Locate the cells, classifying each as a parasitized red blood cell, an uninfected red blood cell, or a white blood cell.
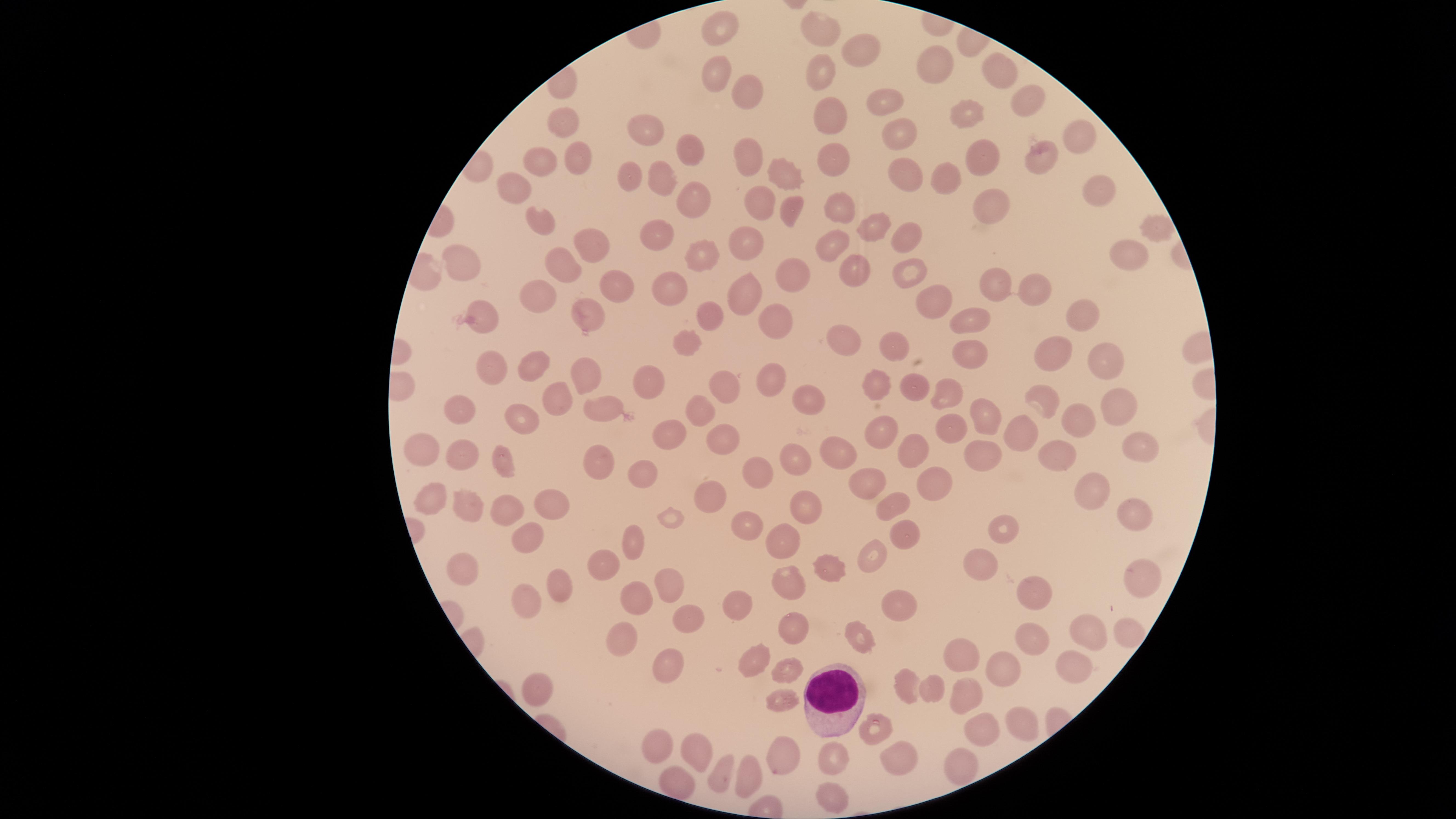

Approximate marker points, in pixels from the top-left corner.
Parasitized red blood cells: (x=876, y=722).
Uninfected red blood cells: (x=724, y=20), (x=823, y=29), (x=858, y=47), (x=933, y=61), (x=714, y=71), (x=818, y=71), (x=1004, y=71), (x=744, y=88), (x=1025, y=92), (x=885, y=104), (x=827, y=110), (x=557, y=115), (x=962, y=116), (x=643, y=127), (x=1081, y=134), (x=898, y=136), (x=682, y=149), (x=748, y=150), (x=987, y=151), (x=1037, y=156), (x=836, y=159), (x=537, y=163), (x=576, y=163), (x=784, y=169), (x=630, y=178), (x=941, y=178), (x=908, y=179), (x=660, y=180), (x=514, y=187), (x=1096, y=192), (x=685, y=194), (x=989, y=200), (x=758, y=205), (x=842, y=209), (x=790, y=213), (x=532, y=215), (x=872, y=228), (x=1157, y=234), (x=656, y=238), (x=905, y=238), (x=587, y=239), (x=835, y=246), (x=743, y=247), (x=707, y=253), (x=1127, y=256), (x=462, y=258), (x=563, y=261), (x=849, y=268), (x=909, y=272), (x=796, y=274), (x=998, y=281), (x=611, y=287), (x=1036, y=290), (x=674, y=291), (x=931, y=300), (x=748, y=302), (x=543, y=304), (x=708, y=314), (x=1084, y=314), (x=586, y=316), (x=488, y=317), (x=776, y=320), (x=966, y=325), (x=849, y=342), (x=693, y=344), (x=893, y=344), (x=971, y=357), (x=1059, y=359), (x=1110, y=366), (x=528, y=367), (x=493, y=368), (x=585, y=375), (x=650, y=378), (x=773, y=379), (x=726, y=382), (x=872, y=383), (x=910, y=391), (x=950, y=391), (x=560, y=398), (x=1045, y=399), (x=799, y=401), (x=1109, y=406), (x=463, y=407), (x=607, y=408), (x=701, y=409), (x=526, y=413), (x=1075, y=417), (x=990, y=418), (x=881, y=431), (x=948, y=431), (x=672, y=435), (x=1135, y=439), (x=1027, y=440), (x=722, y=441), (x=418, y=446), (x=912, y=447), (x=983, y=448), (x=455, y=451), (x=832, y=452), (x=1051, y=456), (x=794, y=458), (x=597, y=462), (x=505, y=465), (x=637, y=471), (x=756, y=477), (x=860, y=478), (x=937, y=485), (x=1089, y=493), (x=712, y=494), (x=426, y=498), (x=550, y=499), (x=1136, y=502), (x=887, y=505), (x=799, y=506), (x=469, y=507), (x=503, y=507), (x=749, y=523), (x=998, y=530), (x=902, y=534), (x=522, y=537), (x=785, y=538), (x=632, y=547), (x=874, y=555), (x=977, y=562), (x=607, y=564), (x=462, y=568), (x=1136, y=568), (x=833, y=569), (x=1036, y=582), (x=673, y=583), (x=785, y=583), (x=556, y=586), (x=634, y=589), (x=530, y=600), (x=742, y=601), (x=897, y=609), (x=686, y=617), (x=793, y=629), (x=1085, y=633), (x=622, y=636), (x=857, y=638), (x=1036, y=641), (x=962, y=660), (x=658, y=661), (x=757, y=665), (x=1073, y=668), (x=1009, y=672), (x=784, y=676), (x=906, y=690), (x=537, y=692), (x=933, y=693), (x=963, y=696), (x=778, y=703), (x=1018, y=722), (x=978, y=731), (x=656, y=742), (x=693, y=749), (x=783, y=751), (x=903, y=754), (x=829, y=761), (x=959, y=767), (x=718, y=774), (x=746, y=774), (x=679, y=782), (x=830, y=792).
White blood cells: (x=826, y=693).

capture = smartphone photograph through the microscope eyepiece
preparation = thin blood smear
image size = 1456×819 pixels
stain = Giemsa
visible region = circular
field of view = single
species = Plasmodium falciparum